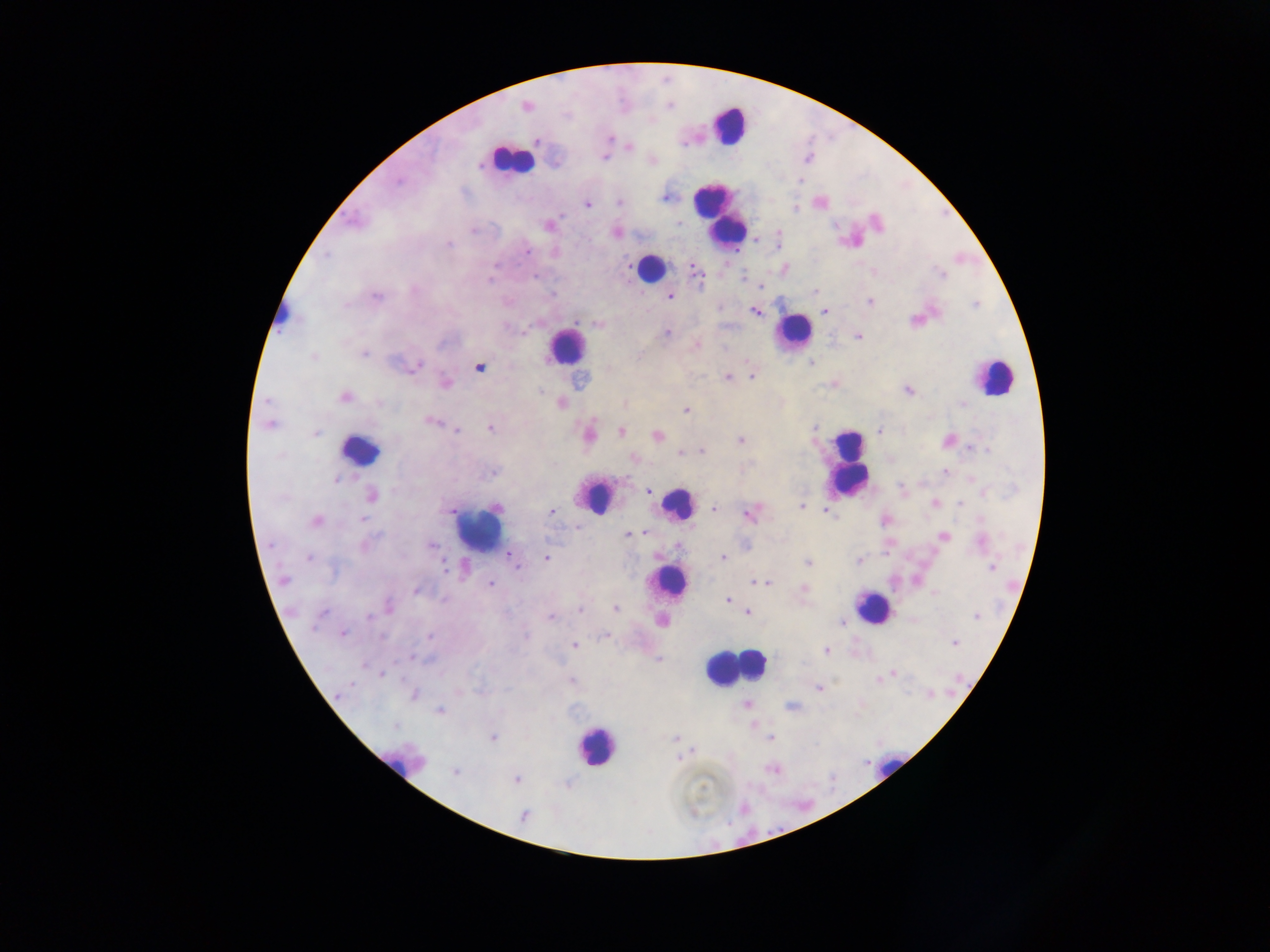

Approximate centers as (x, y) in pixels. Malaria parasite locations: (526, 106), (608, 138), (537, 140), (629, 147), (604, 155), (652, 160), (555, 161), (666, 197), (619, 202), (820, 202), (587, 203), (549, 225), (615, 232), (756, 240), (783, 269), (694, 270), (873, 271), (940, 274), (758, 286), (815, 290), (375, 296), (669, 296), (869, 301), (824, 310), (754, 311), (916, 321), (598, 323), (666, 333), (857, 335), (695, 344), (363, 353), (314, 357), (811, 363), (414, 366), (480, 367), (751, 375), (726, 376), (445, 384), (835, 384), (908, 389), (541, 391), (344, 397), (267, 401), (560, 402), (624, 403), (685, 409), (430, 421), (269, 423), (490, 427), (457, 430), (621, 431), (879, 431), (314, 433), (587, 435), (657, 435), (740, 440), (948, 440), (973, 448), (701, 450), (681, 453), (634, 458), (944, 470), (493, 471), (972, 478), (648, 491), (371, 495), (934, 502), (959, 503), (801, 506), (712, 509), (450, 510), (825, 511), (551, 512), (750, 512), (361, 518), (884, 520), (316, 522), (575, 528), (646, 533), (628, 534), (943, 536), (980, 542), (431, 545), (678, 546), (509, 553), (309, 557), (546, 557), (724, 557), (858, 560), (807, 562), (517, 566), (992, 566), (283, 580), (755, 582), (767, 583), (490, 584), (416, 589), (804, 590), (933, 592), (727, 600), (388, 607), (615, 608), (580, 610), (747, 613), (976, 615), (550, 616), (662, 621), (841, 621), (342, 633), (606, 635), (430, 636), (955, 643), (574, 645), (826, 651), (659, 659), (381, 673), (893, 673), (876, 678), (571, 679), (820, 687), (413, 694), (929, 694), (746, 704), (791, 706), (439, 710), (493, 738), (771, 738), (676, 739), (694, 750), (773, 769), (454, 773), (516, 778), (523, 816). Leukocyte locations: (728, 125), (510, 160), (720, 217), (649, 267), (281, 317), (793, 332), (566, 346), (992, 376), (359, 451), (848, 465), (594, 497), (677, 504), (478, 527), (668, 583), (872, 607), (732, 666), (596, 746), (402, 760), (890, 765). One field of view. Thick blood smear. Sample from Ghana. Image is 1270×952 pixels. Photographed through a microscope with a mobile-phone camera.